Identify the parasite.
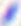

This is Toxoplasma gondii.

{
  "magnification": "400x",
  "modality": "micrograph"
}